State which parasite is depicted.
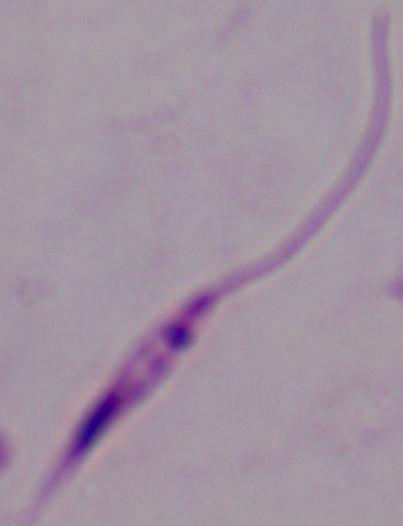
This is Leishmania.

{
  "modality": "micrograph",
  "magnification": "1000x"
}